State the preparation type.
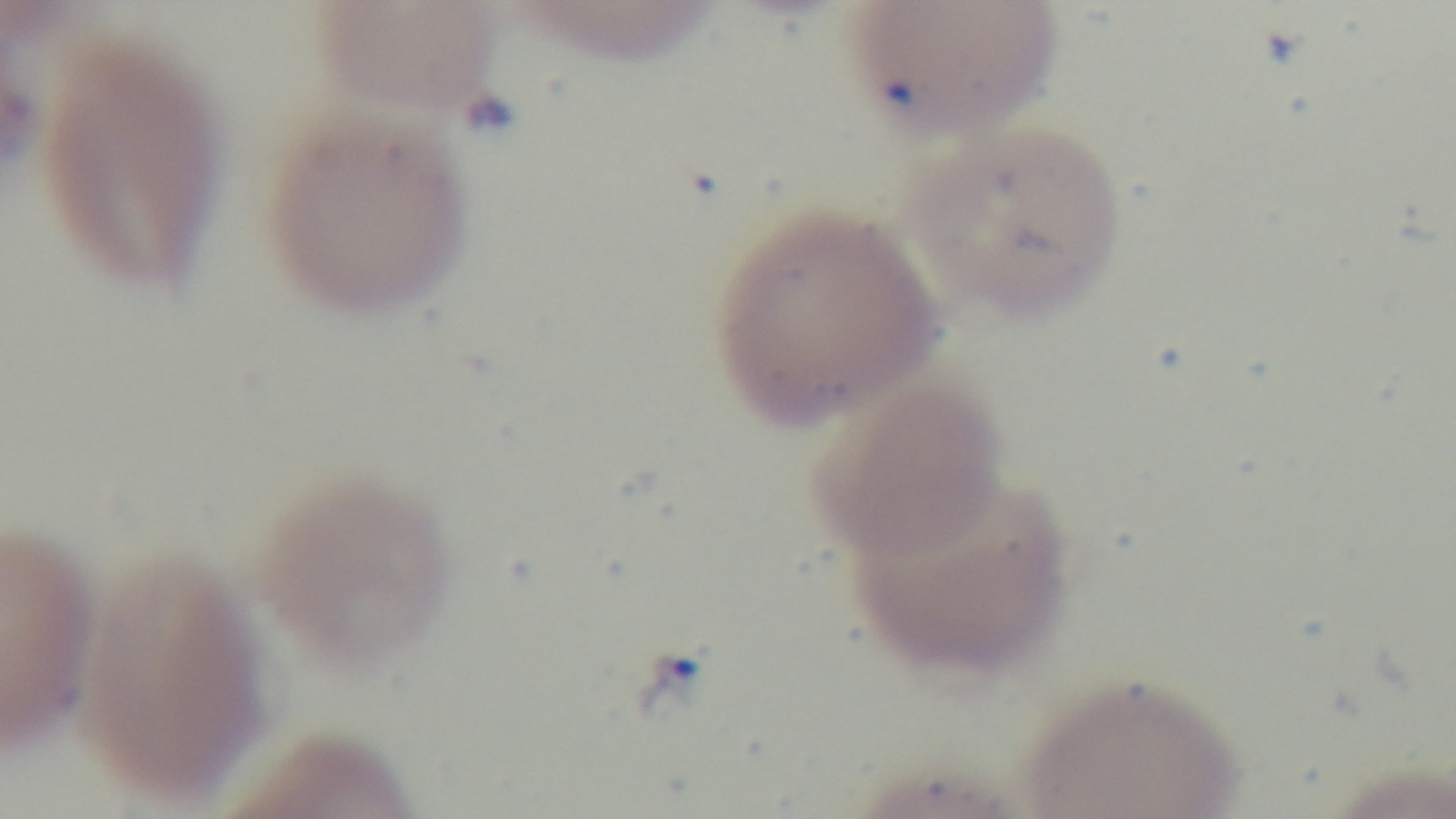
A thin smear.

Giemsa stain. Malaria status: infected. Photomicrograph. Single field of view. Oil-immersion objective, 100x. Mounted 4K digital camera.